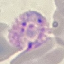

result = malaria parasites identified
preparation = thin smear
stain = Giemsa
capture = smartphone through the microscope eyepiece
image type = automatically extracted cell patch, resized to 64 × 64 pixels